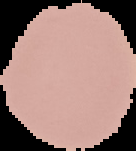
preparation = thin blood film
result = negative for malaria parasites
image type = cell region segmented out of the field of view; surrounding area masked to black
image size = 136×151 pixels